Report the malaria status of this cell.
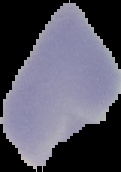
It is uninfected.

Summary:
  - Image size: 121×172 pixels
  - Preparation: thin blood smear
  - Image type: cell region segmented out of the field of view; surrounding area masked to black